Assess this cell for malaria.
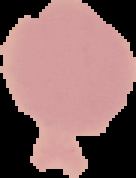
It is uninfected.

preparation = thin blood smear
image type = segmented cell region with the area outside set to black
image size = 136×178 pixels